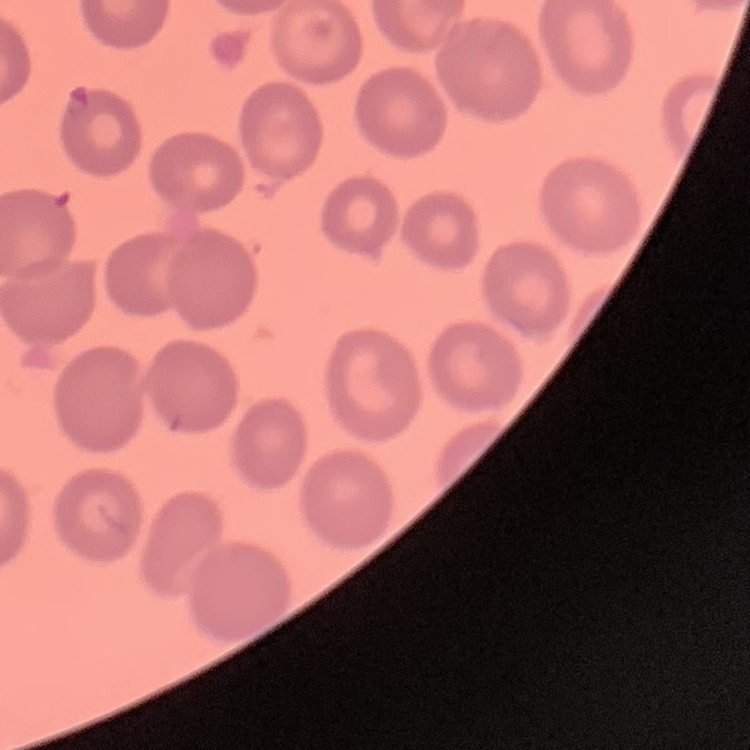

The red blood cells exhibit no rouleaux formation. One tile cut from a larger photomicrograph. Thin peripheral smear. Field's or Giemsa stain.